Give the position of every Plasmodium falciparum parasite, noting its life-cycle stage.
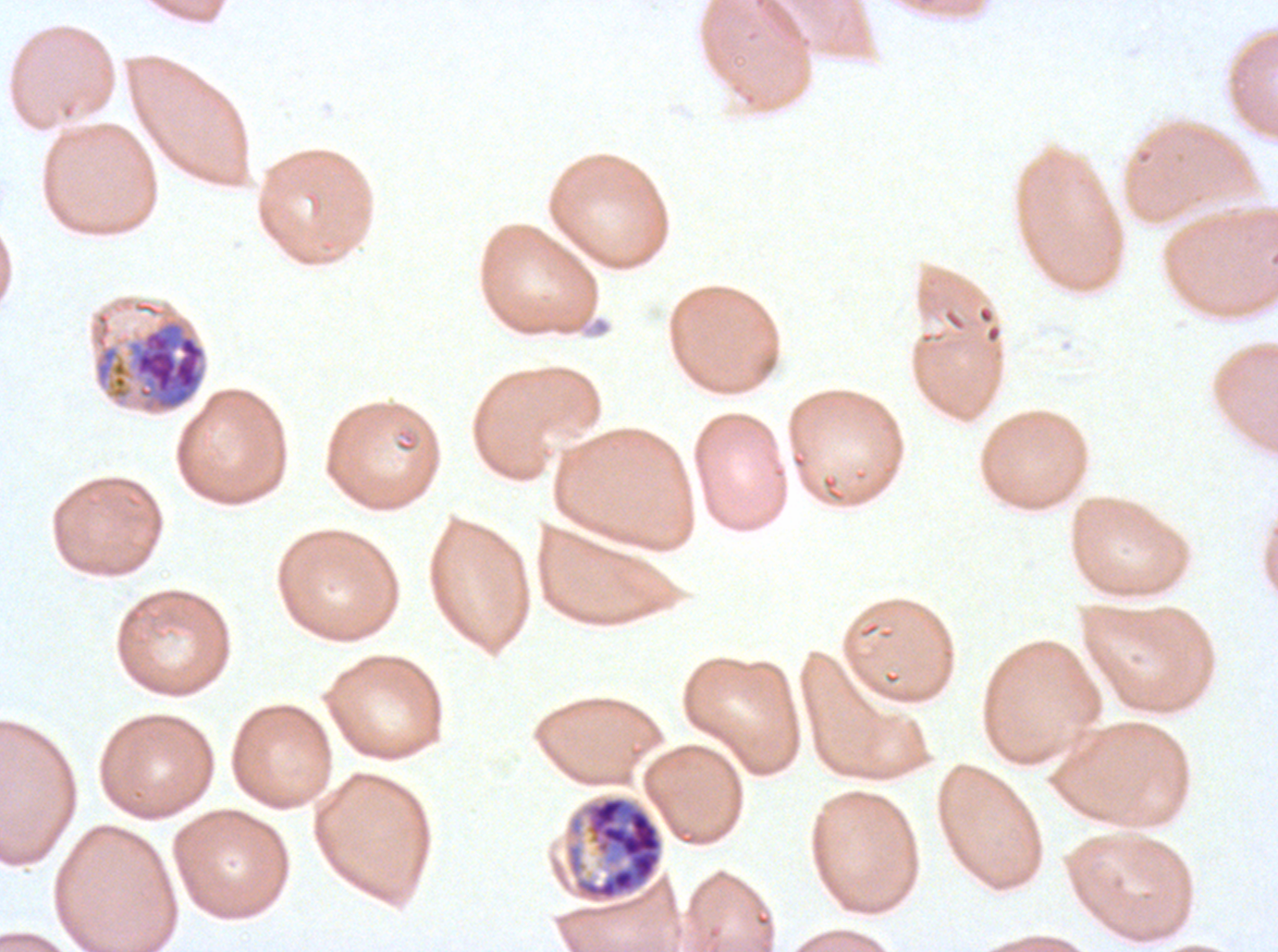

Approximate bounding boxes as [x1, y1, x2, y2] in pixels.
Late trophozoites: [90, 299, 208, 415].
Late schizonts: [564, 794, 665, 904].
No rings, late-ring/early-trophozoite forms, mid trophozoites, early schizonts, segmenters, or gametocytes observed.

Giemsa stain. A sub-image separated from a larger composite. Plasmodium falciparum cultured ex vivo for 24 to 48 hours, from a patient in The Gambia. Life-cycle stages observed: late trophozoite, late schizont. Image is 1278×952 pixels. Thin blood film.